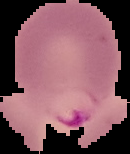 From a thin blood smear. Image is 130×154 pixels. Malaria status: parasitized. Segmented cell region on a black background.